Evaluate for malaria.
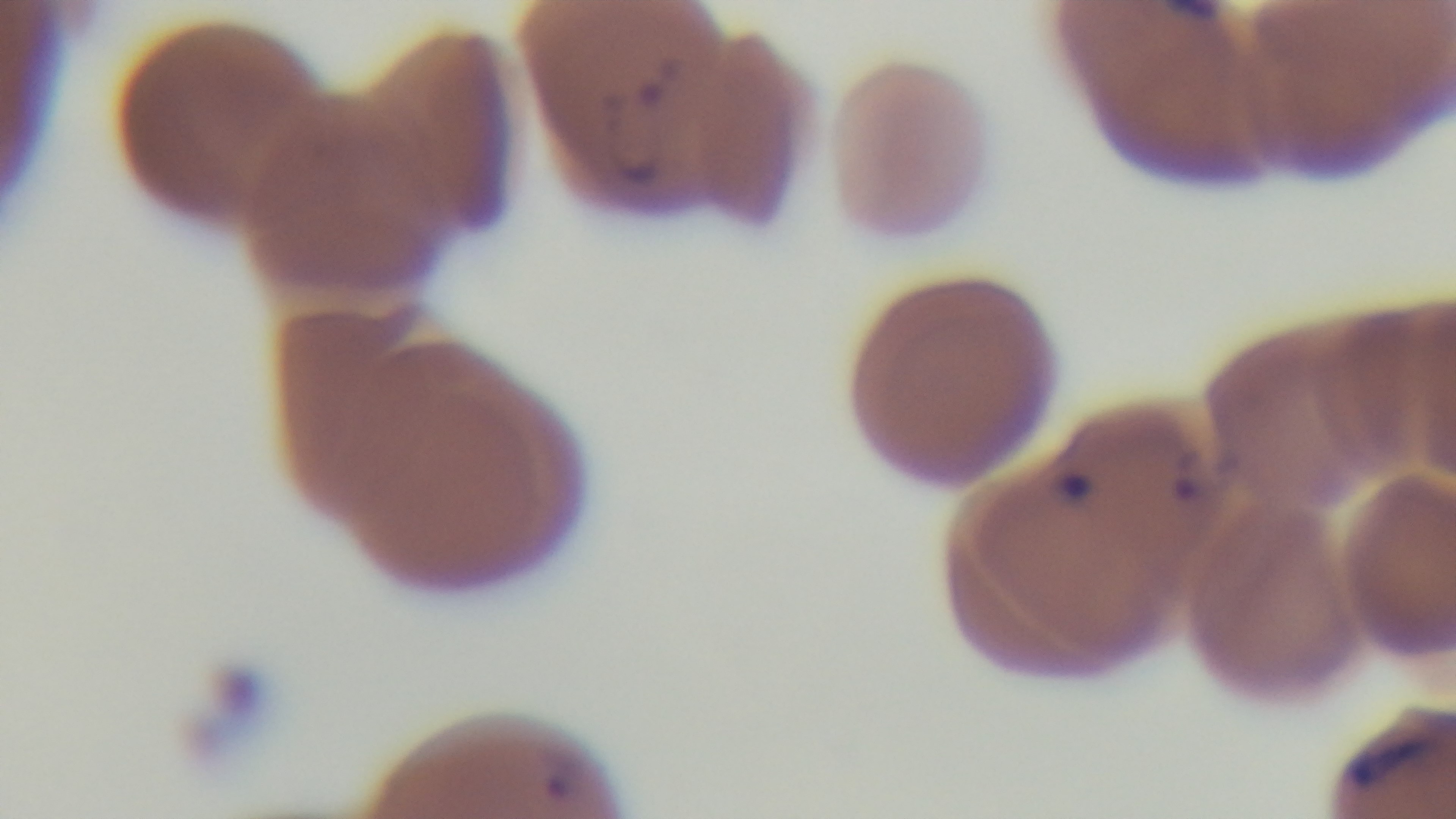

Positive.

stain = Giemsa
capture = mounted 4K digital camera
modality = light microscopy
objective = 100x oil immersion
field of view = one from the slide
preparation = thin